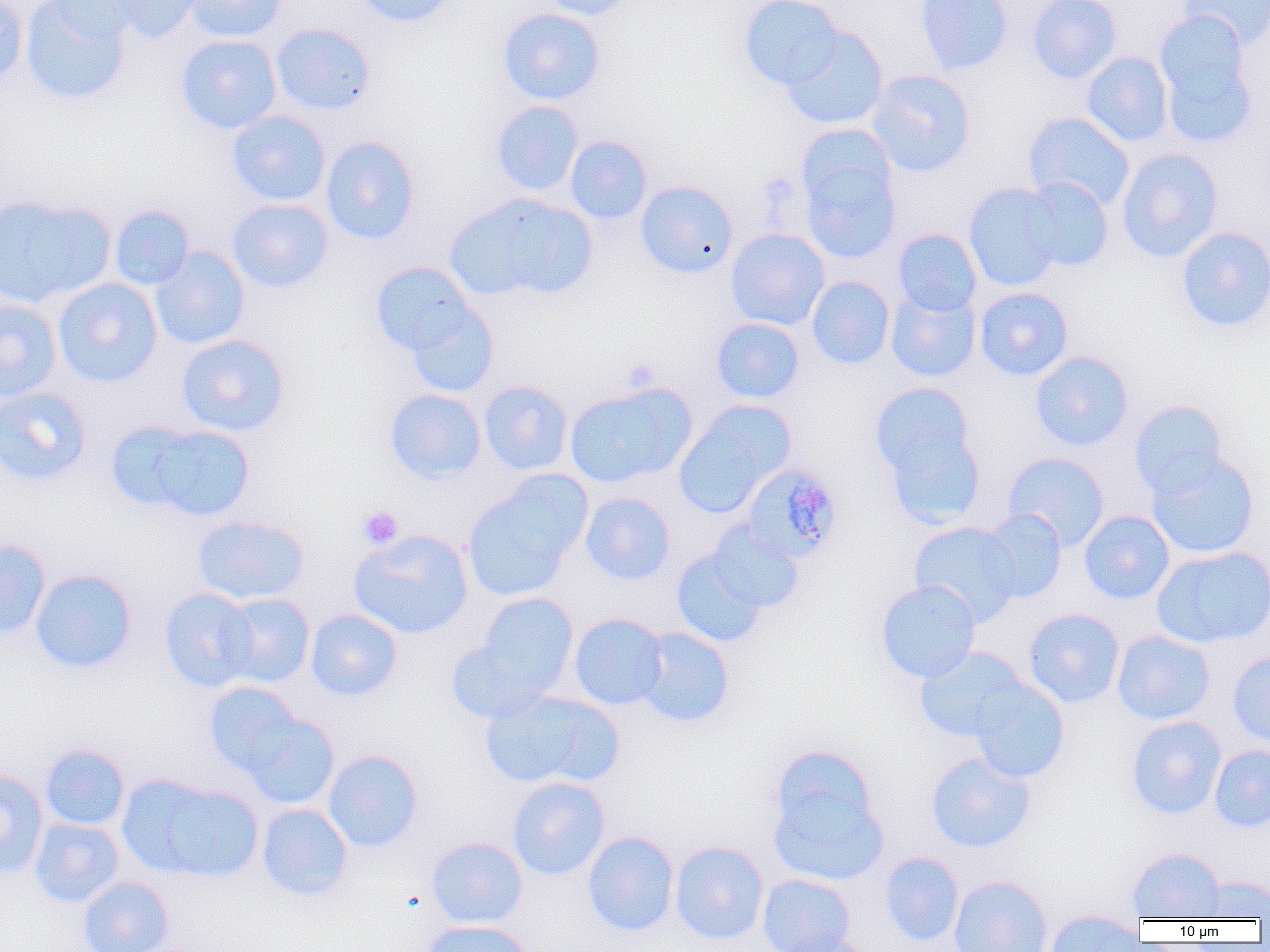

Summary:
  - Coordinate format: approximate bounding boxes as [x1, y1, x2, y2] in pixels
  - Platelet locations: [622, 357, 660, 392], [358, 505, 404, 549]
  - Plasmodium malariae-infected red blood cell locations: [740, 461, 844, 563]
  - Uninfected red blood cell locations: [0, 0, 29, 87], [20, 0, 131, 107], [44, 0, 149, 44], [103, 0, 206, 44], [183, 0, 287, 43], [353, 0, 458, 28], [537, 0, 641, 20], [738, 0, 845, 91], [915, 0, 1013, 76], [1027, 0, 1120, 84], [1177, 0, 1270, 48], [497, 7, 606, 105], [1153, 10, 1258, 146], [270, 23, 376, 115], [780, 25, 889, 130], [175, 34, 282, 135], [1081, 51, 1174, 147], [865, 70, 976, 177], [490, 101, 583, 196], [226, 110, 331, 207], [1023, 112, 1135, 211], [795, 124, 896, 212], [320, 136, 421, 245], [565, 136, 652, 224], [1116, 148, 1223, 263], [800, 156, 901, 264], [1020, 177, 1113, 273], [635, 180, 738, 278], [963, 183, 1065, 292], [445, 193, 598, 304], [0, 194, 116, 308], [227, 198, 334, 294], [109, 205, 194, 290], [1176, 227, 1270, 333], [725, 228, 830, 330], [893, 229, 982, 316], [150, 246, 250, 350], [369, 262, 481, 361], [806, 276, 895, 369], [52, 277, 163, 388], [886, 287, 981, 383], [974, 287, 1073, 381], [0, 297, 63, 403], [403, 299, 499, 398], [711, 318, 805, 404], [176, 334, 290, 437], [1030, 351, 1134, 451], [478, 380, 574, 475], [870, 381, 979, 499], [564, 382, 696, 488], [0, 386, 91, 487], [384, 388, 486, 484], [1129, 400, 1228, 500], [673, 402, 794, 517], [119, 421, 255, 521], [1146, 451, 1260, 559], [1003, 453, 1110, 550], [462, 480, 584, 602], [580, 492, 676, 585], [979, 509, 1067, 603], [1079, 510, 1175, 604], [193, 515, 310, 605], [907, 521, 1023, 627], [705, 522, 804, 615], [348, 529, 474, 640], [0, 539, 51, 639], [1151, 546, 1270, 648], [671, 547, 768, 647], [29, 568, 138, 674], [875, 580, 981, 683], [159, 587, 258, 693], [217, 593, 315, 688], [476, 593, 579, 694], [1023, 608, 1125, 708], [305, 609, 402, 702], [569, 613, 668, 710], [634, 627, 734, 729], [1112, 629, 1215, 725], [445, 637, 552, 724], [914, 646, 1028, 742], [1227, 649, 1270, 749], [970, 680, 1069, 784], [204, 681, 307, 778], [479, 689, 618, 790], [239, 712, 339, 809], [1126, 715, 1227, 820], [40, 744, 129, 830], [766, 745, 887, 881], [1209, 745, 1270, 832], [322, 749, 423, 852], [925, 751, 1036, 853], [0, 769, 48, 878], [126, 776, 264, 881], [507, 776, 610, 880], [257, 804, 353, 901], [29, 817, 124, 908], [582, 831, 679, 936], [426, 837, 528, 928], [669, 840, 769, 944], [1127, 848, 1225, 921], [880, 851, 964, 946], [757, 873, 856, 951], [948, 874, 1053, 952], [1192, 875, 1269, 919], [77, 876, 174, 952], [1043, 909, 1145, 952], [421, 920, 534, 952], [773, 930, 873, 952]
  - Slide-level diagnosis: Plasmodium malariae
  - Preparation: thin blood smear
  - Field of view: one of a larger specimen
  - Image size: 1270×952 pixels
  - Modality: optical microscopy
  - Magnification: 1000x